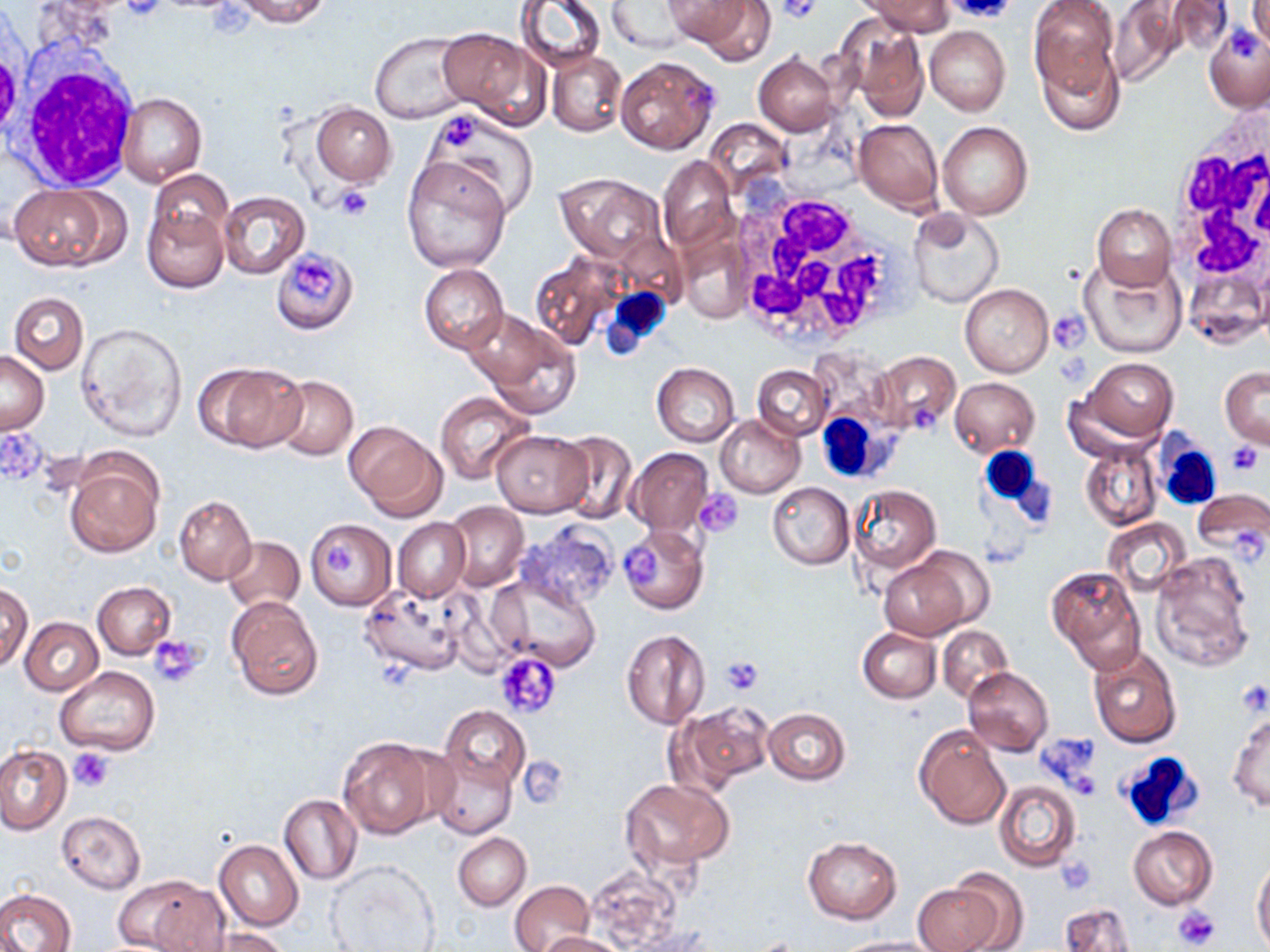

slide-level diagnosis = no evidence of blood parasites
stain = May-Grünwald-Giemsa
modality = optical microscopy
preparation = thin blood film
field of view = one of a larger specimen
magnification = 1000x
image size = 1270×952 pixels
uninfected red blood cell locations = approximate bounding boxes as (x1,y1)-(x2,y2) corner pairs in pixels: (233,0)-(330,26), (514,0)-(605,72), (670,0)-(775,61), (866,0)-(953,35), (1028,0)-(1120,95), (608,1)-(697,54), (1162,1)-(1236,59), (1111,2)-(1190,84), (1244,4)-(1268,56), (1204,24)-(1270,113), (850,25)-(929,122), (925,26)-(1010,116), (438,28)-(547,126), (368,30)-(479,124), (1037,47)-(1124,134), (0,48)-(21,140), (547,51)-(626,135), (615,54)-(720,155), (753,54)-(840,136), (118,92)-(206,186), (311,103)-(395,186), (424,110)-(540,218), (853,118)-(944,213), (926,121)-(1021,304), (938,121)-(1034,220), (400,155)-(510,274), (658,156)-(738,256), (147,170)-(233,253), (554,173)-(669,265), (12,183)-(121,272), (218,192)-(309,279), (144,204)-(229,292), (1092,204)-(1176,290), (907,207)-(1004,308), (275,248)-(355,331), (1080,256)-(1188,359), (532,257)-(620,351), (419,264)-(508,354), (959,283)-(1054,377), (9,292)-(88,374), (466,311)-(579,415), (76,321)-(189,442), (0,350)-(49,434), (872,350)-(961,436), (1077,357)-(1179,446), (196,362)-(306,452), (651,363)-(739,446), (752,364)-(831,440), (1220,367)-(1269,448), (270,375)-(358,459), (950,377)-(1039,456), (434,390)-(535,484), (716,414)-(805,499), (347,423)-(446,519), (492,430)-(593,516), (552,430)-(638,523), (1080,440)-(1162,532), (627,449)-(712,536), (64,455)-(162,557), (767,482)-(854,569), (848,485)-(941,577), (1193,487)-(1269,563), (174,495)-(256,584), (444,502)-(528,590), (392,518)-(470,602), (1103,518)-(1191,596), (304,519)-(396,611), (514,523)-(620,611), (616,525)-(707,614), (222,535)-(305,612), (1149,550)-(1256,671), (877,552)-(980,639), (1048,567)-(1146,672), (492,573)-(599,671), (92,581)-(176,659), (1,582)-(33,670), (362,586)-(469,676), (226,597)-(323,700), (19,617)-(103,694), (858,627)-(941,703), (937,627)-(1012,703), (621,628)-(711,729), (1088,646)-(1183,750), (54,665)-(159,756), (963,667)-(1054,755), (676,700)-(772,792), (440,706)-(529,791), (763,708)-(851,785), (1227,710)-(1269,812), (915,726)-(1010,828), (337,736)-(444,839), (0,746)-(71,834), (429,752)-(517,838), (620,778)-(733,869), (993,781)-(1079,872), (279,795)-(361,885), (58,811)-(146,894), (1128,826)-(1217,910), (453,832)-(531,910), (802,837)-(901,923), (214,839)-(303,930), (324,859)-(440,952), (1252,862)-(1270,949), (584,863)-(685,947), (946,869)-(1029,949), (123,875)-(226,952), (510,880)-(593,952), (912,881)-(1003,952), (0,888)-(76,952), (1060,902)-(1136,952), (209,929)-(292,952), (534,932)-(627,952), (834,937)-(936,952)
platelet locations = approximate bounding boxes as (x1,y1)-(x2,y2) corner pairs in pixels: (121,0)-(166,22), (777,0)-(820,23), (942,1)-(1018,23), (1225,26)-(1260,58), (684,78)-(719,115), (444,118)-(476,145), (332,184)-(375,220), (292,255)-(338,299), (1048,310)-(1090,353), (1226,441)-(1264,475), (698,490)-(743,535), (1230,525)-(1267,561), (320,544)-(360,577), (622,545)-(659,584), (150,635)-(206,687), (494,651)-(562,719), (719,657)-(763,694), (1239,679)-(1269,716), (1037,732)-(1101,790), (68,748)-(115,792), (518,758)-(567,808), (1069,772)-(1101,800), (1056,856)-(1097,894), (1174,904)-(1220,948)
white blood cell locations = approximate bounding boxes as (x1,y1)-(x2,y2) corner pairs in pixels: (17,58)-(140,189), (1165,104)-(1270,314), (720,184)-(914,349), (599,287)-(673,359), (819,412)-(881,483), (1149,432)-(1226,510), (979,447)-(1042,505), (1114,751)-(1206,833)